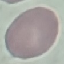 Malaria status: uninfected. Cell patch, automatically extracted from a larger field of view and resized to 64 × 64 pixels. Photographed with a smartphone camera at the microscope eyepiece. Thin blood film. Giemsa-stained preparation.